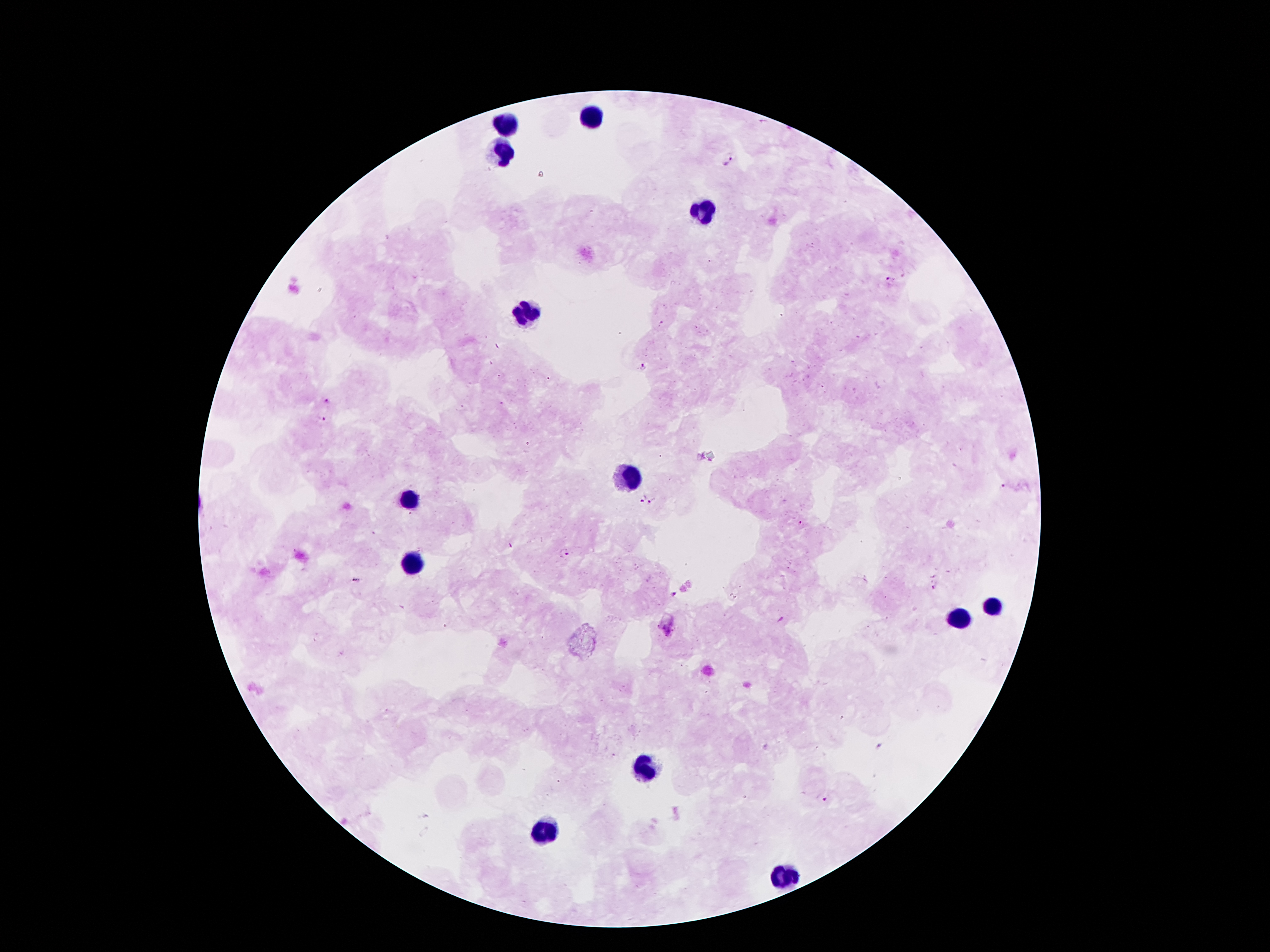 Photographed through the microscope eyepiece with a smartphone camera. Giemsa stain. Patient malaria status: positive for Plasmodium falciparum. Thick blood film. 100x magnification. One field from this slide. Image is 1270×952 pixels.